Assess this cell for malaria.
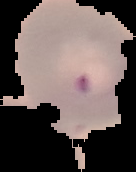
It is parasitized.

preparation = thin blood smear
image type = cell region segmented out of the field of view; surrounding area masked to black
image size = 136×172 pixels